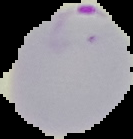
Summary:
  - Image type: segmented cell region on a black background
  - Image size: 133×139 pixels
  - Malaria status: parasitized
  - Preparation: thin blood film